Report the malaria status of this cell.
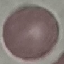
Uninfected.

Summary:
  - Image type: cell patch, automatically extracted from a larger field of view and resized to 64 × 64 pixels
  - Capture: smartphone camera at the microscope eyepiece
  - Preparation: thin blood film
  - Stain: Giemsa